Point out each malaria parasite.
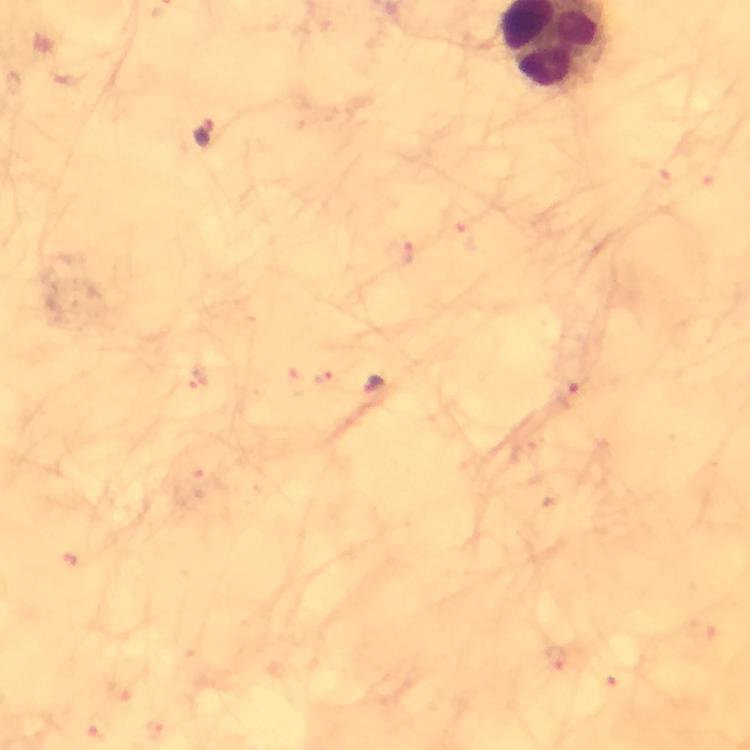

Approximate centers as [x, y] in pixels.
Malaria parasites: [202, 134], [405, 254], [326, 379], [374, 386], [569, 394].

immersion oil = used
cropped from = one field of view
stain = Giemsa
magnification = 100x
preparation = thick smear
image size = 750×750 pixels
capture = smartphone mounted on the microscope
context = from a diagnostic examination for malaria